Identify the parasite.
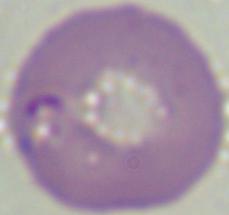

This is Babesia.

modality = photomicrograph
magnification = 1000x